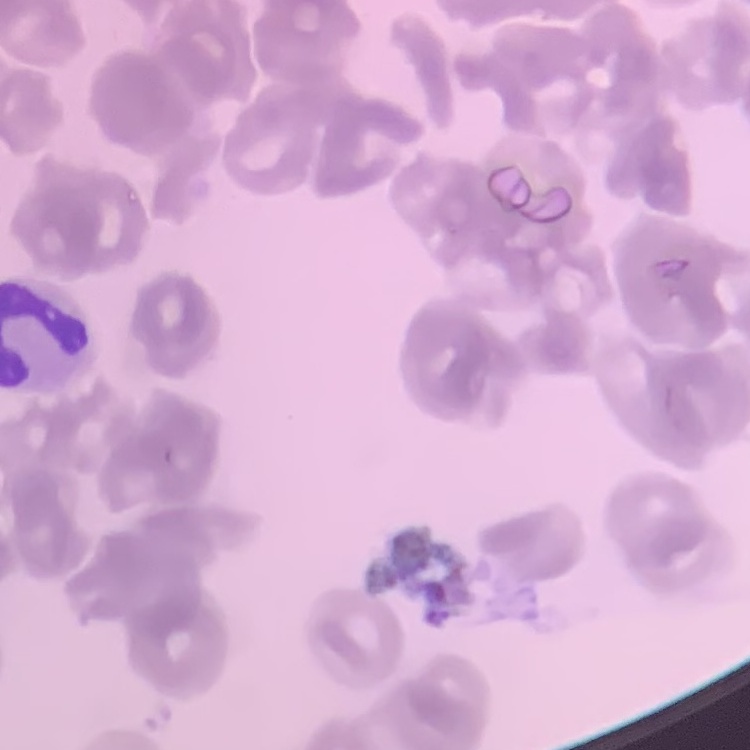

Summary:
  - Erythrocyte morphology: rouleaux formation
  - Image type: square crop of a larger photomicrograph
  - Preparation: thin blood smear
  - Stain: Field's or Giemsa